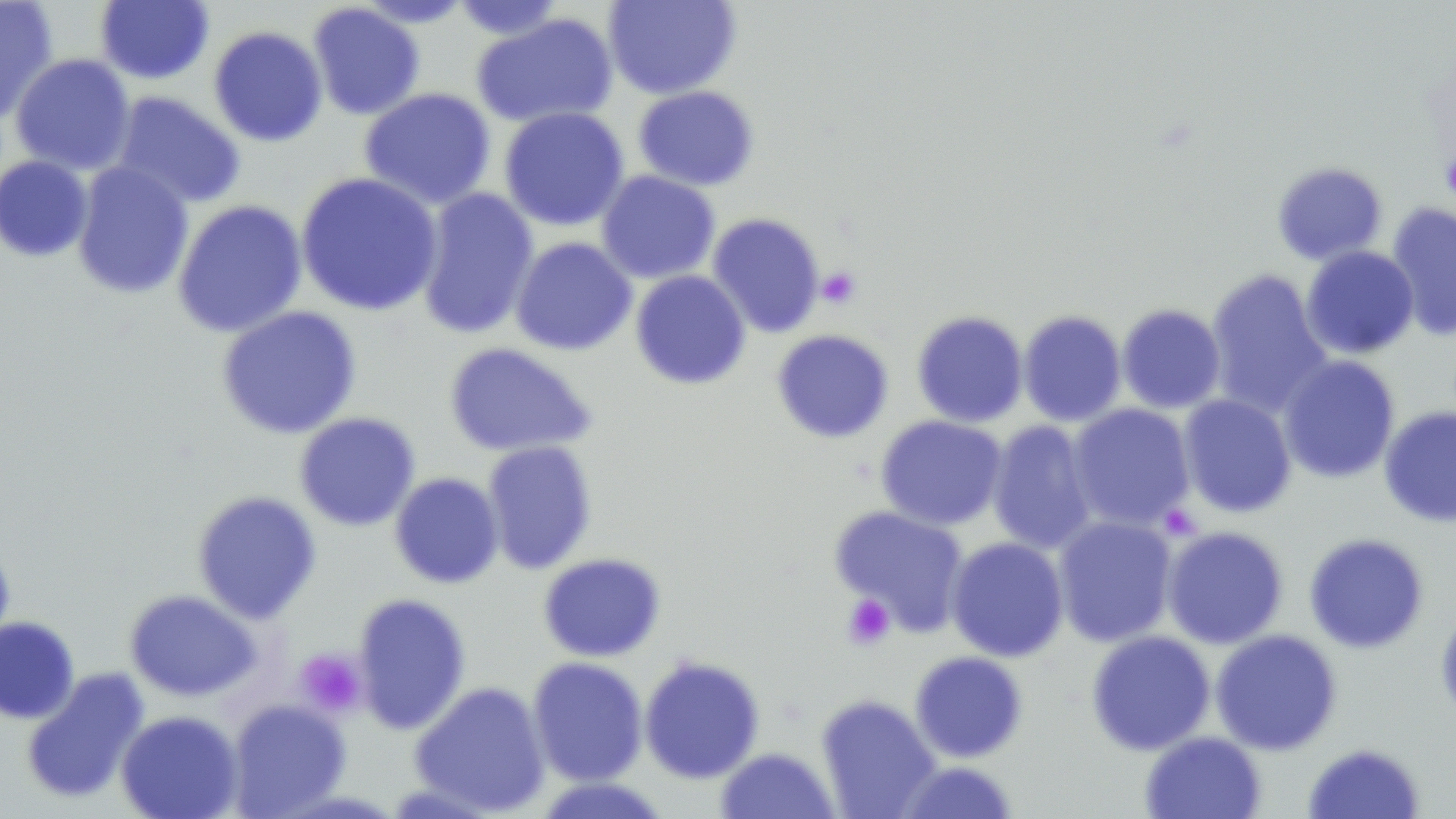

Approximate bounding boxes as (x1,y1)-(x2,y2) corner pairs in pixels. Uninfected red blood cell locations: (0,0)-(59,125), (354,0)-(475,27), (451,0)-(567,40), (603,0)-(741,99), (95,1)-(214,84), (307,3)-(425,120), (471,13)-(618,129), (208,25)-(328,147), (10,53)-(135,176), (632,85)-(759,191), (358,87)-(496,209), (110,91)-(246,209), (498,106)-(629,232), (0,155)-(94,262), (1272,161)-(1388,265), (72,162)-(194,299), (596,170)-(721,284), (295,171)-(443,317), (416,188)-(540,340), (172,199)-(308,338), (1386,201)-(1456,341), (706,212)-(826,338), (511,237)-(637,356), (1301,246)-(1419,358), (1205,268)-(1333,419), (630,270)-(751,390), (1116,304)-(1226,414), (216,305)-(362,439), (912,310)-(1028,427), (1018,310)-(1127,427), (771,329)-(894,443), (443,342)-(597,458), (1278,355)-(1401,483), (1177,394)-(1297,518), (1066,403)-(1196,532), (1379,406)-(1456,527), (294,412)-(420,531), (876,415)-(1008,530), (986,420)-(1099,555), (482,440)-(597,574), (389,471)-(504,589), (192,490)-(322,624), (829,505)-(970,637), (1053,515)-(1178,647), (1161,525)-(1289,649), (1304,532)-(1429,654), (946,536)-(1069,662), (0,541)-(15,656), (538,553)-(665,662), (124,589)-(262,702), (352,593)-(471,735), (1436,605)-(1456,725), (0,616)-(79,724), (1210,629)-(1342,755), (1086,630)-(1216,755), (909,651)-(1028,763), (527,656)-(649,786), (639,656)-(765,783), (20,667)-(149,805), (409,680)-(551,817), (816,694)-(941,818), (226,699)-(351,818), (116,710)-(244,818), (1140,731)-(1266,819), (1302,743)-(1426,818), (715,747)-(840,818), (895,760)-(1019,818), (531,776)-(673,818). Platelet locations: (1440,144)-(1456,207), (817,266)-(861,309), (842,593)-(895,650), (295,648)-(366,718). Slide-level diagnosis: no evidence of blood parasites. Optical microscopy. 1000x magnification. May-Grünwald-Giemsa stain. Image is 1456×819 pixels. One field of a larger specimen. Thin blood smear.